Give a bounding box for every artifact (platelet-like body, stain precipitate, or debris).
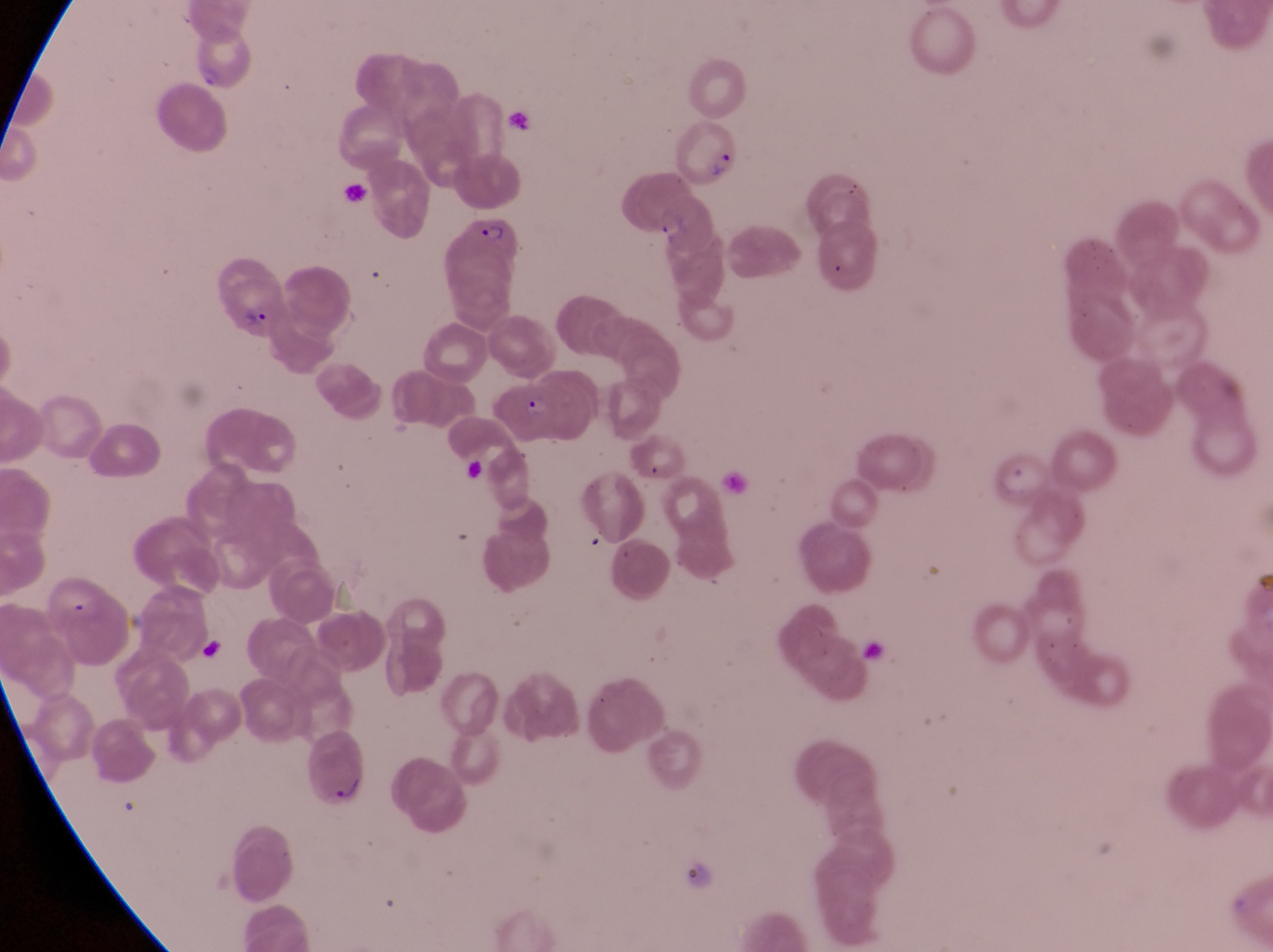

Approximate bounding boxes as {left, top, right, bottom} in pixels.
Artifacts (platelet-like body, stain precipitate, or debris): {194, 632, 226, 665}.

Parasitised red blood cell locations: {669, 123, 748, 192}, {449, 217, 523, 325}, {213, 260, 290, 340}, {500, 375, 565, 447}. Photographed through the eyepiece of an Olympus CX-23 microscope with a smartphone camera. Collected in Uganda. Image is 1273×952 pixels. Single field of view. At a magnification of 1000x. Thin blood film.